Classify this cell by malaria status.
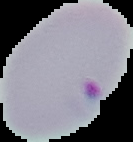
It is parasitized.

Cell region segmented out of the field of view; the surrounding area is masked to black. From a thin blood smear. Image is 133×142 pixels.